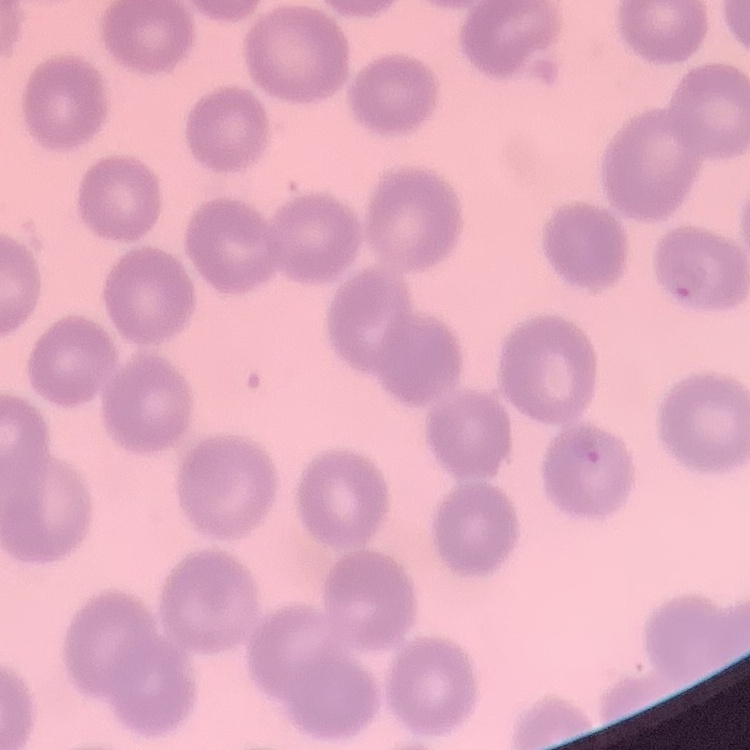
{
  "erythrocyte_morphology": "no rouleaux formation",
  "stain": "Field's or Giemsa",
  "preparation": "thin blood film",
  "image_type": "square crop of a larger photomicrograph"
}